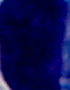
Summary:
  - Identification: white blood cell
  - Modality: micrograph
  - Magnification: 1000x